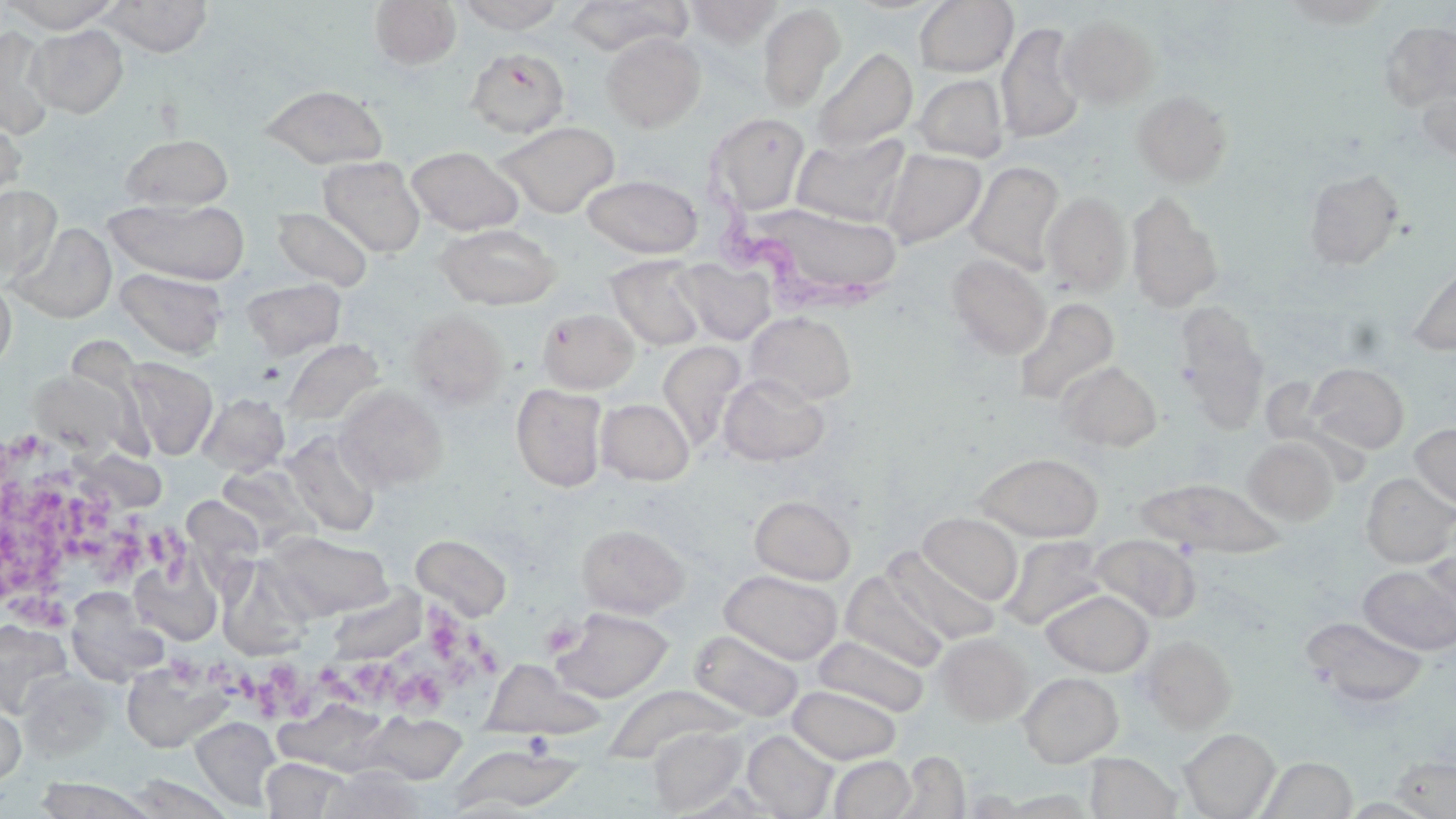

Summary:
  - Coordinate format: approximate bounding boxes as (x1,y1)-(x2,y2) corner pairs in pixels
  - Uninfected red blood cell locations: (2,0)-(120,32), (99,0)-(214,57), (455,0)-(566,33), (567,0)-(691,56), (914,0)-(1018,77), (1277,0)-(1395,28), (368,1)-(462,70), (685,1)-(782,47), (757,3)-(846,113), (1058,14)-(1159,110), (1380,21)-(1456,111), (996,22)-(1085,144), (26,24)-(128,118), (0,26)-(55,140), (600,31)-(706,131), (811,46)-(917,153), (465,47)-(570,138), (912,74)-(1008,162), (1416,82)-(1456,162), (261,84)-(388,168), (1132,89)-(1234,188), (706,112)-(811,216), (0,114)-(25,211), (494,120)-(620,218), (792,132)-(911,226), (120,133)-(233,211), (407,146)-(524,235), (879,149)-(986,248), (319,156)-(426,257), (965,161)-(1065,272), (1303,168)-(1405,269), (582,174)-(702,259), (0,185)-(61,285), (1041,191)-(1130,296), (1126,192)-(1223,312), (106,198)-(250,284), (751,203)-(903,305), (272,206)-(373,291), (9,222)-(117,323), (435,223)-(562,309), (946,253)-(1051,360), (607,256)-(707,350), (677,257)-(776,345), (1405,259)-(1456,356), (115,268)-(227,357), (0,275)-(16,374), (242,278)-(346,360), (1013,297)-(1120,405), (1175,303)-(1269,425), (406,308)-(510,409), (538,308)-(639,393), (745,311)-(857,406), (280,338)-(383,428), (657,341)-(745,450), (123,358)-(218,459), (1058,360)-(1162,451), (1307,362)-(1410,453), (28,368)-(143,460), (719,373)-(830,465), (511,383)-(608,492), (334,384)-(448,491), (198,392)-(290,476), (596,398)-(695,485), (1410,422)-(1456,512), (282,430)-(382,538), (1243,437)-(1340,524), (975,452)-(1103,541), (216,463)-(315,546), (1361,472)-(1456,568), (1136,478)-(1285,558), (749,495)-(856,585), (918,512)-(1022,605), (576,523)-(688,619), (266,531)-(394,619), (411,534)-(511,620), (1091,534)-(1199,622), (1001,536)-(1109,629), (1420,539)-(1456,631), (885,547)-(999,646), (129,556)-(224,645), (1358,564)-(1456,655), (719,569)-(842,664), (840,570)-(947,672), (66,589)-(169,686), (1041,589)-(1153,675), (551,607)-(673,702), (1303,616)-(1429,710), (0,620)-(72,717), (688,629)-(804,722), (934,632)-(1033,725), (812,634)-(929,717), (1138,635)-(1238,732), (122,659)-(232,753), (16,670)-(114,762), (1018,671)-(1123,767), (788,685)-(901,764), (0,695)-(26,787), (363,712)-(466,784), (190,716)-(281,810), (647,725)-(747,814), (1179,728)-(1280,818), (742,729)-(838,818), (450,746)-(586,814), (1084,752)-(1182,819), (829,755)-(915,818), (1391,755)-(1456,818), (1256,756)-(1356,818), (261,758)-(351,818), (319,766)-(430,819), (122,773)-(236,818), (32,777)-(158,818), (997,790)-(1099,818)
  - Trypanosoma brucei locations: (706,185)-(894,320)
  - Platelet locations: (4,439)-(129,586), (98,510)-(198,585), (3,584)-(87,635), (386,597)-(503,715), (544,605)-(586,656), (166,648)-(249,702), (233,653)-(323,730), (315,659)-(395,717)
  - Slide-level diagnosis: Trypanosoma brucei
  - Magnification: 1000x
  - Field of view: one of a larger specimen
  - Preparation: thin blood film
  - Stain: May-Grünwald-Giemsa
  - Image size: 1456×819 pixels
  - Modality: optical microscopy